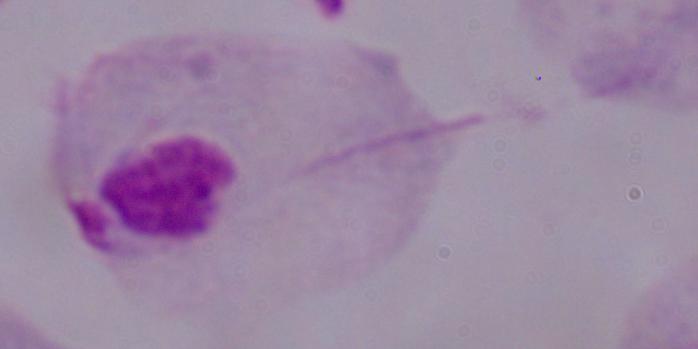

modality = photomicrograph
identification = trichomonad
magnification = 1000x